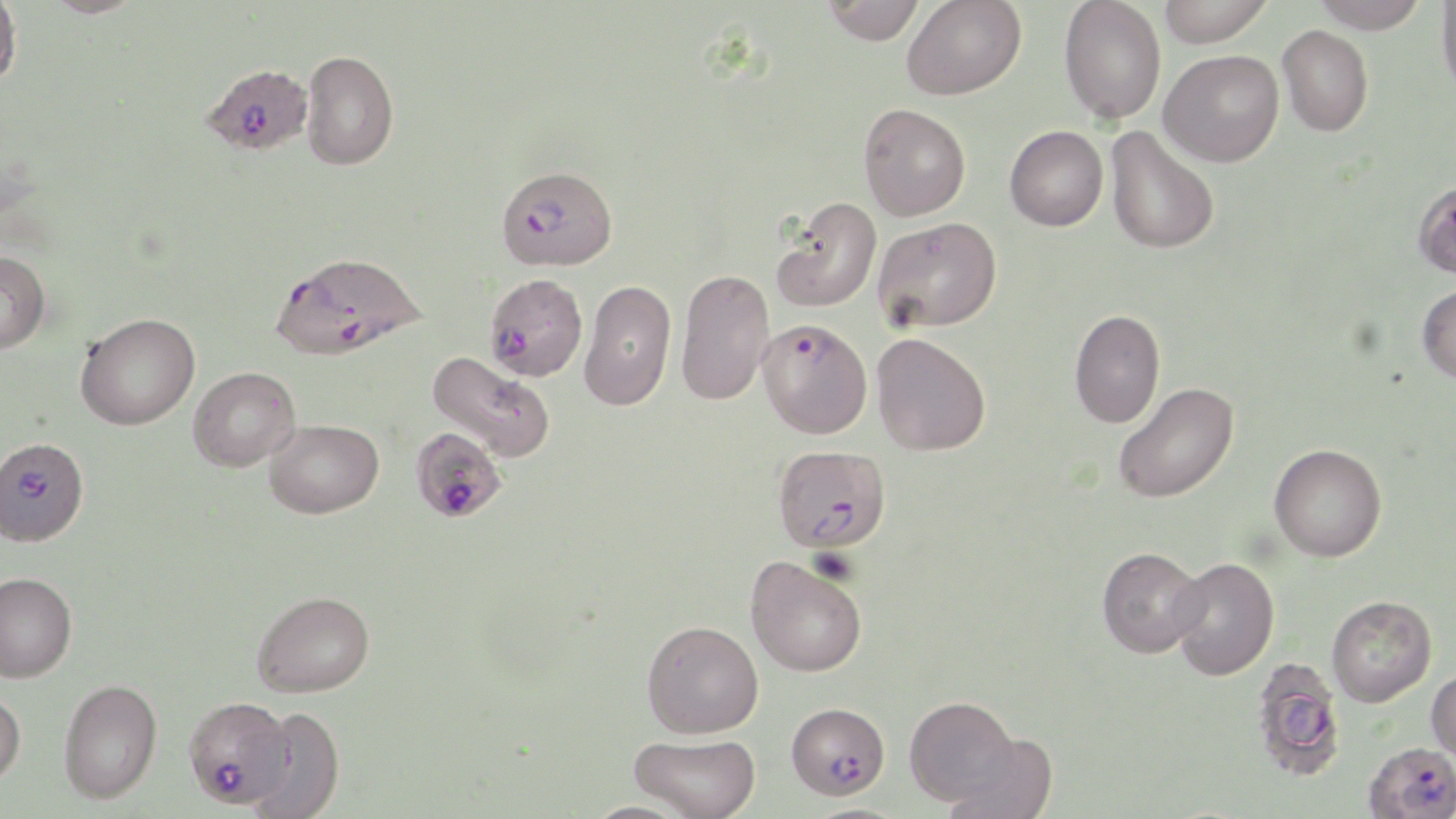
slide-level diagnosis = Plasmodium falciparum
magnification = 1000x
uninfected red blood cell locations = approximate bounding boxes as [x1, y1, x2, y2] in pixels: [0, 0, 22, 90], [41, 0, 145, 18], [821, 0, 925, 44], [901, 0, 1026, 100], [1059, 0, 1166, 124], [1158, 0, 1273, 47], [1311, 0, 1430, 33], [1436, 1, 1456, 101], [1277, 25, 1373, 136], [1159, 49, 1284, 167], [301, 50, 398, 171], [858, 103, 970, 221], [1004, 125, 1108, 231], [1105, 126, 1219, 255], [1411, 179, 1456, 280], [771, 197, 882, 313], [873, 216, 1002, 332], [0, 250, 51, 353], [675, 268, 775, 406], [580, 278, 676, 411], [1416, 283, 1456, 383], [1069, 309, 1165, 428], [76, 312, 200, 430], [871, 332, 991, 456], [427, 351, 556, 463], [188, 366, 300, 471], [1112, 381, 1240, 503], [264, 419, 384, 518], [1269, 443, 1387, 561], [1097, 546, 1206, 658], [745, 554, 867, 677], [1169, 557, 1279, 680], [0, 571, 77, 683], [252, 590, 375, 697], [1327, 595, 1437, 706], [642, 619, 764, 738], [1250, 658, 1347, 781], [1427, 667, 1456, 766], [58, 678, 162, 803], [0, 689, 26, 789], [904, 695, 1021, 805], [244, 705, 346, 819], [939, 731, 1058, 819], [629, 733, 761, 819]
preparation = thin blood film
field of view = single
image size = 1456×819 pixels
modality = light microscopy
Plasmodium falciparum-infected red blood cell locations = approximate bounding boxes as [x1, y1, x2, y2] in pixels: [206, 61, 314, 153], [496, 164, 617, 271], [271, 254, 437, 367], [484, 272, 588, 381], [758, 318, 872, 439], [1, 434, 87, 549], [416, 436, 508, 522], [773, 444, 891, 553], [183, 696, 293, 808], [786, 701, 890, 799], [1363, 743, 1456, 819]
stain = May-Grünwald-Giemsa